Comment on the morphology of the erythrocytes.
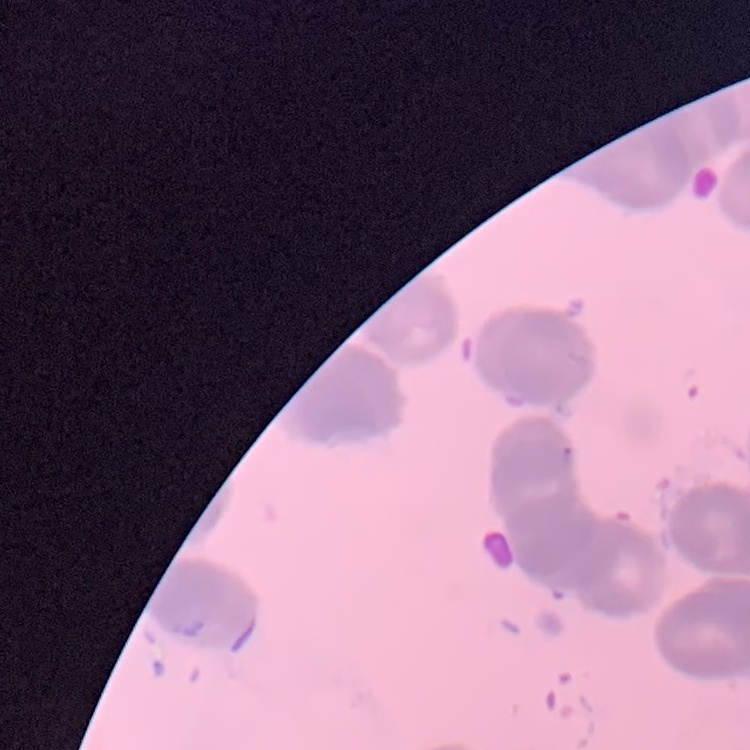
They show rouleaux formation.

image_type: square crop of a larger photomicrograph
stain: Field's or Giemsa
preparation: thin blood film